Classify this cell by malaria status.
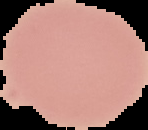

It is uninfected.

Summary:
  - Preparation: thin blood smear
  - Image type: segmented cell region on a black background
  - Image size: 148×130 pixels